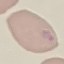
Result: malaria parasites identified. Thin smear of blood. Automatically extracted cell patch, resized to 64 × 64 pixels. Giemsa-stained preparation. Photographed with a smartphone camera at the microscope eyepiece.